Classify this cell by malaria status.
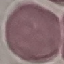

It is uninfected.

Summary:
  - Preparation: thin blood smear
  - Image type: automatically extracted cell patch, resized to 64 × 64 pixels
  - Capture: smartphone camera at the microscope eyepiece
  - Stain: Giemsa